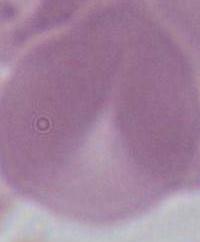

Summary:
  - Magnification: 1000x
  - Modality: photomicrograph
  - Identification: erythrocyte